Comment on the morphology of the erythrocytes.
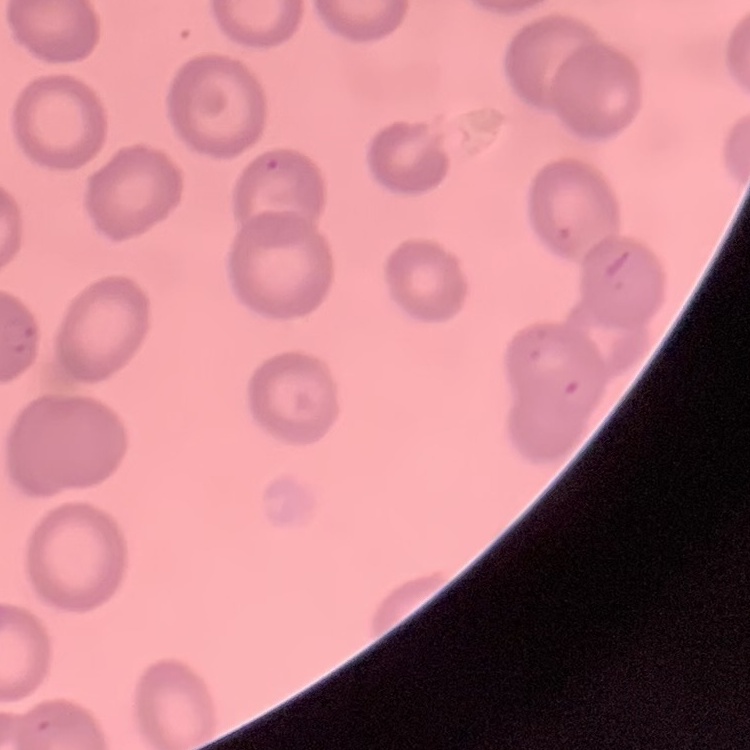
They show no rouleaux formation.

Summary:
  - Image type: square crop of a larger photomicrograph
  - Stain: Field's or Giemsa
  - Preparation: thin blood film